Look for Plasmodium parasites.
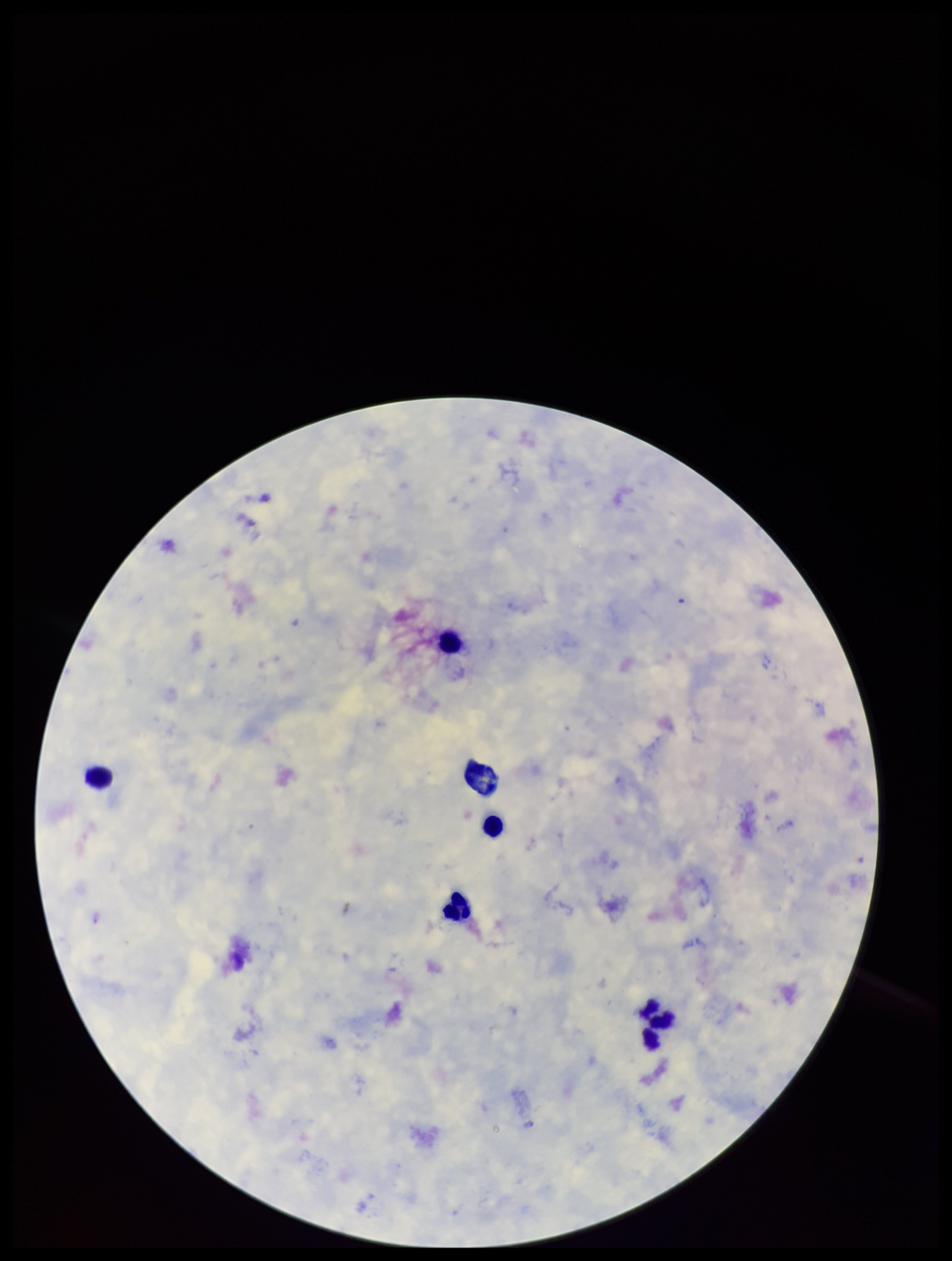

None detected.

Image is 952×1261 pixels. Single field of view. Parasite count: 0. Patient malaria status: negative. Leukocyte count: 6. Giemsa stain. Preparation: thick blood smear. Smartphone photograph taken through the eyepiece of a microscope.